Point out each Plasmodium parasite.
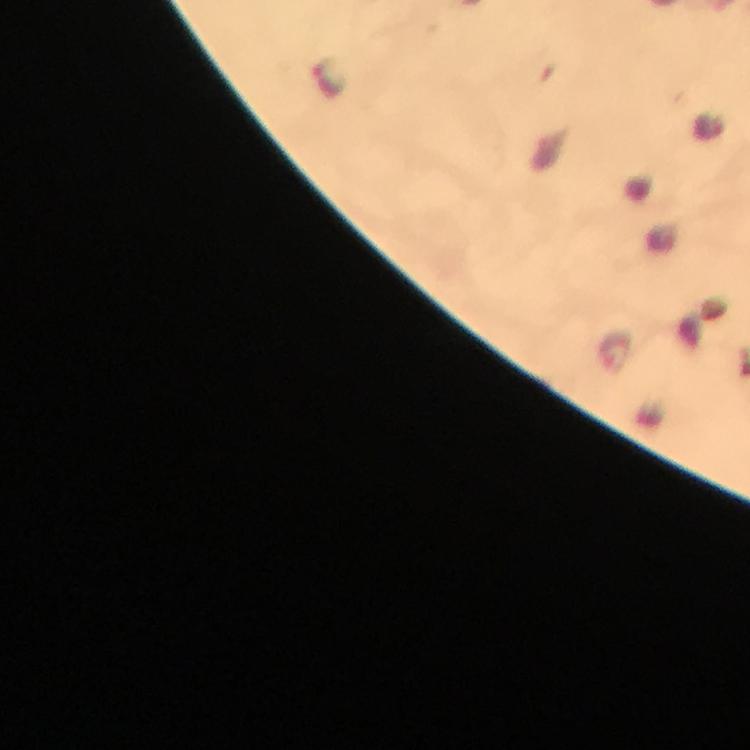

Approximate centers as {x, y} in pixels.
Plasmodium parasites: {326, 80}.

preparation: thick smear
context: from a malaria diagnostic workup
image_size: 750×750 pixels
stain: Giemsa
magnification: 100x
cropped_from: a single field of view
immersion_oil: applied
capture: smartphone photograph through a microscope